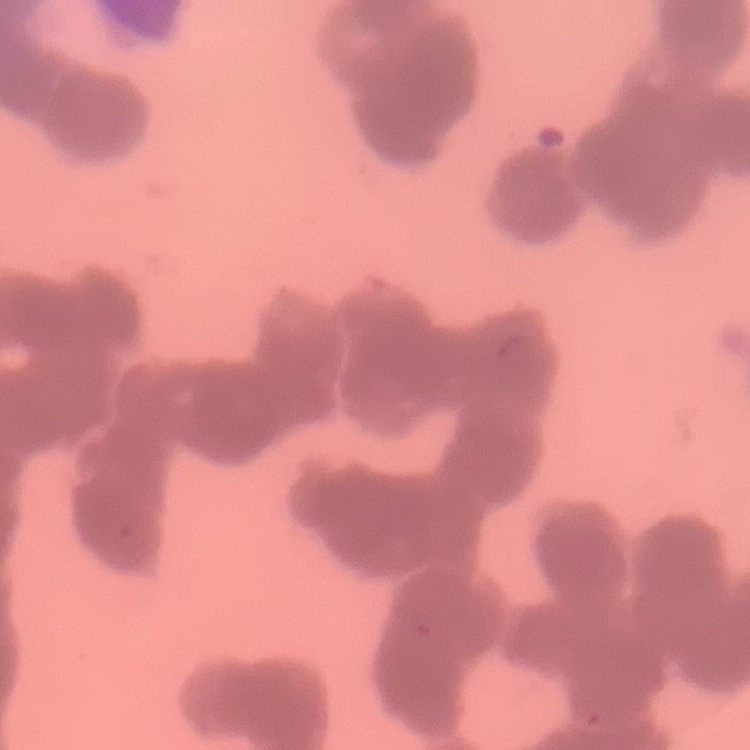
Summary:
  - Erythrocyte morphology: rouleaux formation
  - Preparation: thin blood film
  - Stain: Field's or Giemsa
  - Image type: square crop of a larger photomicrograph